Report the malaria status.
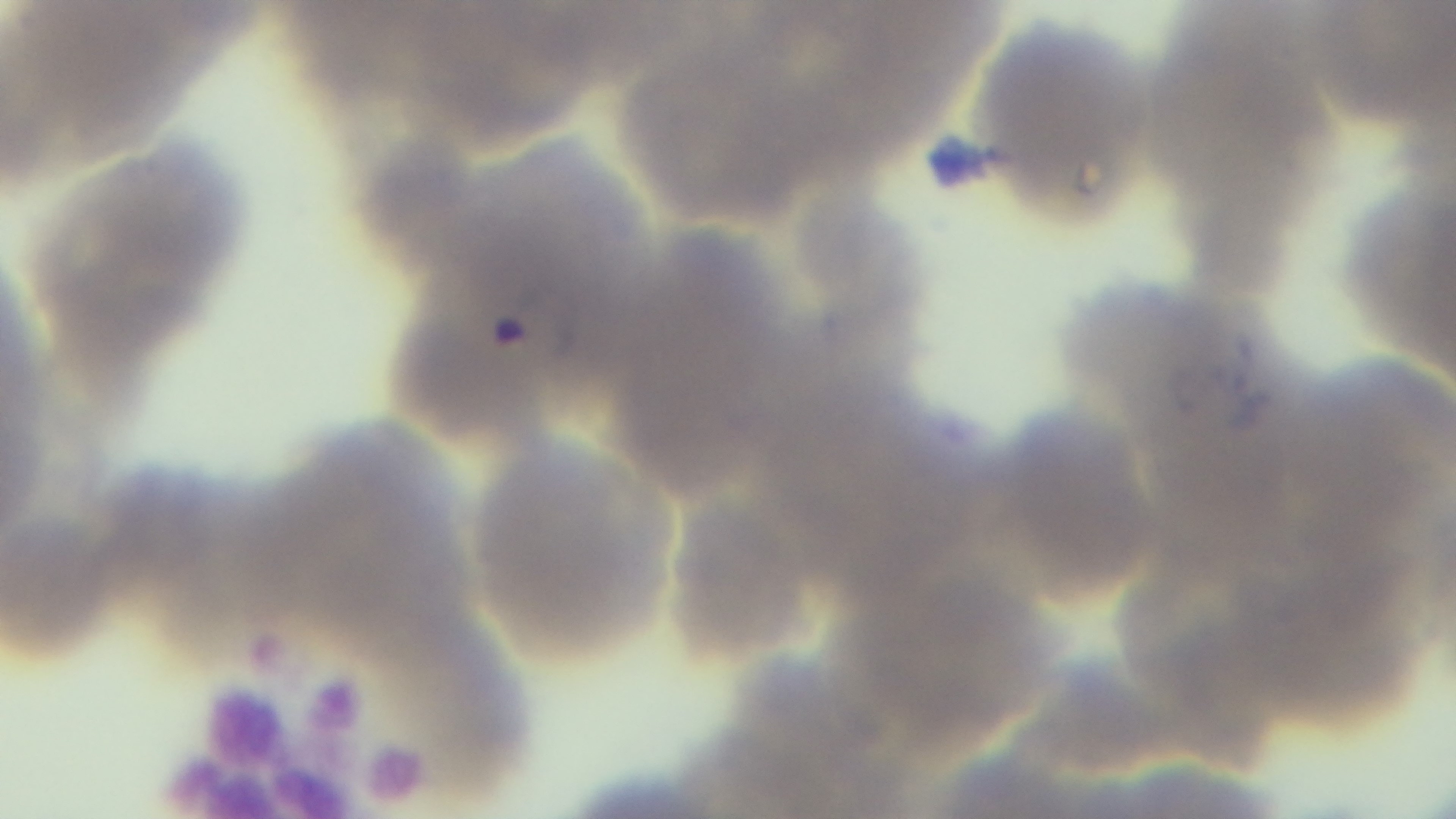
Positive.

Preparation: thin. Oil-immersion objective, 100x. One field from the slide. Photomicrograph. Captured with a mounted 4K digital camera. Giemsa-stained.